Describe the morphology of the red blood cells.
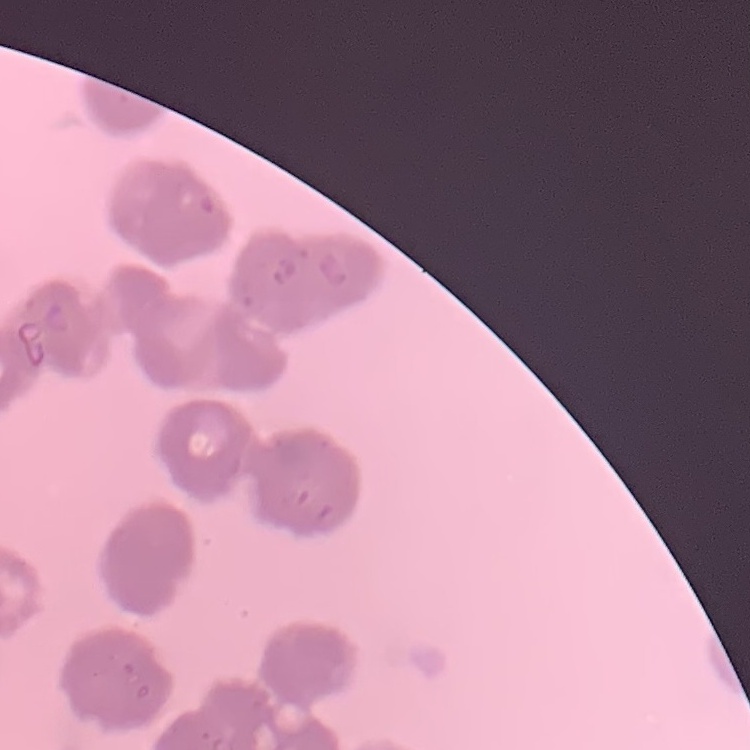
Rouleaux formation.

Summary:
  - Preparation: thin peripheral smear
  - Image type: one tile cut from a larger photomicrograph
  - Stain: Field's or Giemsa